Identify the blood parasite species.
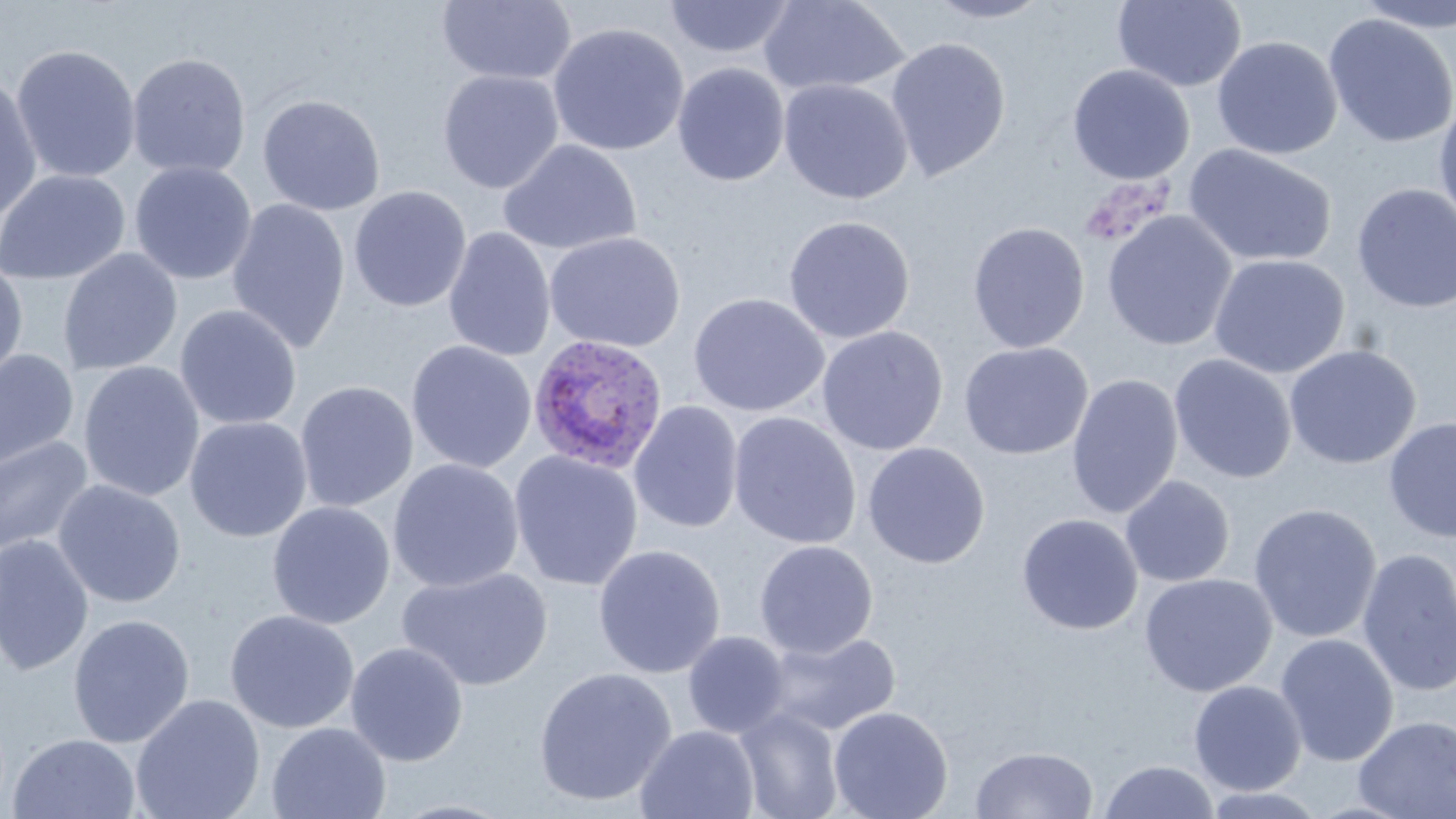

Plasmodium ovale.

preparation: thin blood smear
plasmodium_ovale_infected_red_blood_cell_locations: 'approximate bounding boxes as [x1, y1, x2, y2] in pixels: [527, 334, 669, 476]'
image_size: 1456×819 pixels
uninfected_red_blood_cell_locations: 'approximate bounding boxes as [x1, y1, x2, y2] in pixels: [436, 0, 577, 85], [662, 0, 798, 59], [758, 0, 909, 96], [1112, 0, 1247, 92], [923, 1, 1054, 24], [1351, 1, 1456, 35], [1323, 13, 1456, 148], [547, 22, 690, 156], [884, 36, 1012, 182], [1211, 36, 1342, 160], [10, 43, 142, 183], [126, 53, 251, 179], [672, 63, 790, 186], [1066, 64, 1195, 184], [437, 69, 564, 193], [0, 72, 42, 227], [778, 78, 914, 205], [257, 94, 386, 216], [1433, 98, 1456, 230], [497, 138, 642, 257], [1183, 144, 1337, 268], [130, 161, 257, 285], [0, 169, 131, 285], [1351, 183, 1456, 313], [348, 186, 472, 312], [226, 198, 351, 354], [1102, 210, 1237, 351], [783, 215, 916, 344], [967, 222, 1090, 353], [443, 227, 556, 362], [545, 231, 686, 353], [58, 248, 183, 376], [1208, 254, 1349, 378], [0, 259, 29, 389], [688, 292, 830, 417], [174, 304, 302, 430], [816, 326, 949, 456], [405, 340, 537, 473], [958, 341, 1093, 460], [1284, 344, 1421, 469], [0, 347, 79, 476], [1168, 353, 1297, 484], [77, 361, 205, 503], [1067, 374, 1183, 520], [295, 380, 418, 513], [628, 400, 744, 534], [728, 411, 862, 550], [184, 416, 313, 542], [1383, 416, 1456, 542], [0, 435, 95, 558], [862, 442, 991, 569], [508, 450, 644, 592], [387, 458, 524, 593], [1120, 475, 1236, 587], [52, 479, 187, 609], [267, 501, 395, 630], [1248, 503, 1382, 643], [1016, 513, 1143, 635], [0, 534, 95, 676], [754, 539, 878, 659], [593, 544, 726, 679], [1356, 548, 1456, 698], [398, 565, 553, 691], [1139, 572, 1277, 697], [224, 609, 360, 734], [67, 614, 195, 748], [761, 629, 902, 737], [682, 631, 791, 740], [1275, 633, 1399, 767], [345, 641, 469, 767], [533, 666, 677, 807], [1188, 680, 1307, 795], [130, 693, 266, 819], [828, 706, 954, 819], [733, 707, 845, 819], [1353, 715, 1456, 818], [266, 722, 392, 819], [635, 725, 761, 819], [7, 733, 141, 819], [970, 746, 1099, 819], [1098, 759, 1219, 818], [1201, 786, 1329, 818], [383, 799, 520, 819]'
magnification: 1000x
field_of_view: single
stain: May-Grünwald-Giemsa
modality: optical microscopy